Assess for Plasmodium parasites.
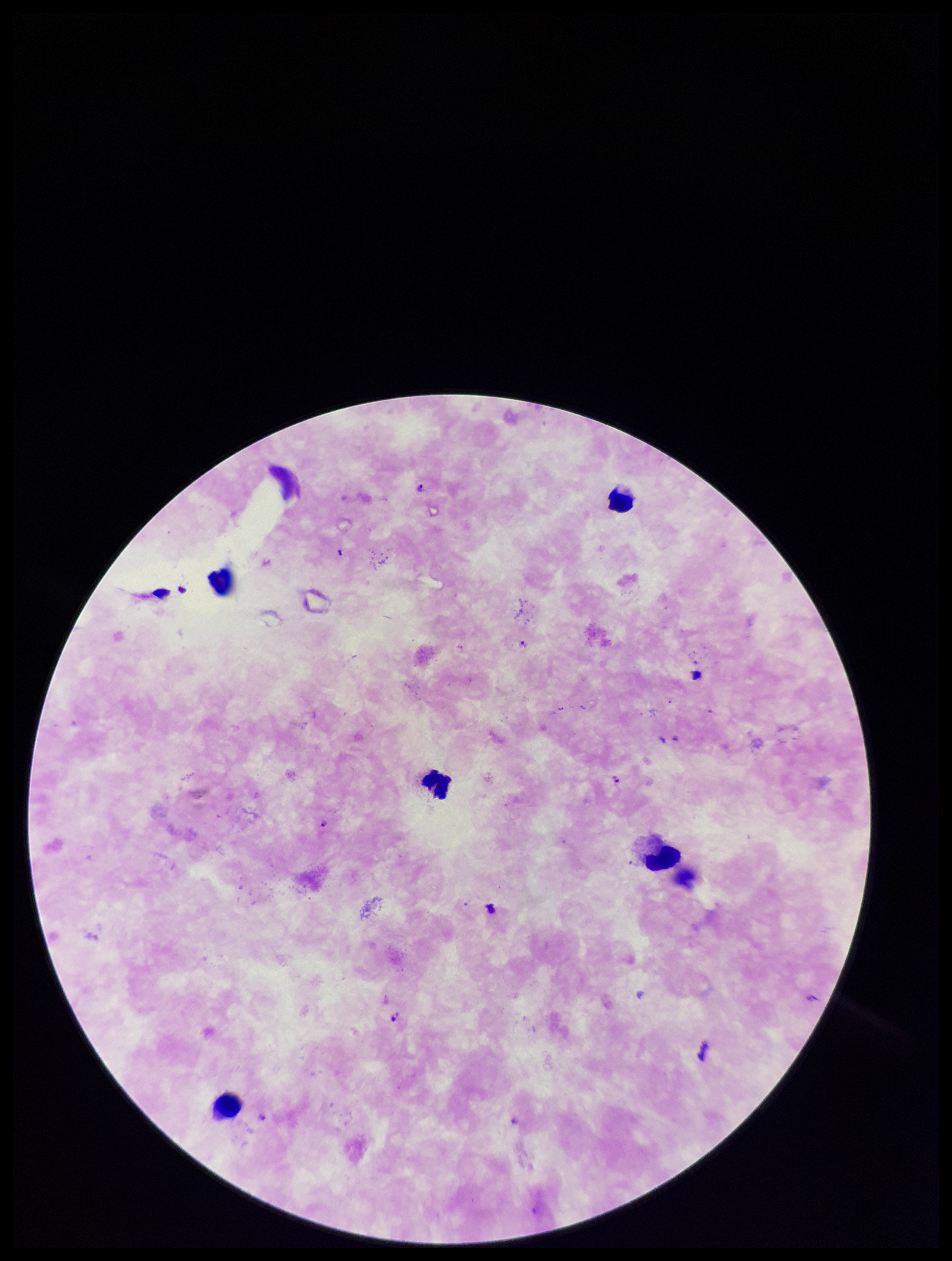
Identified.

Preparation: thick smear. Image is 952×1261 pixels. Species reported for this patient: Plasmodium falciparum. Patient malaria status: infected. Giemsa stain. One field from this slide. Parasite count: 4. Photographed through the microscope eyepiece with a smartphone camera. Leukocyte count: 5.